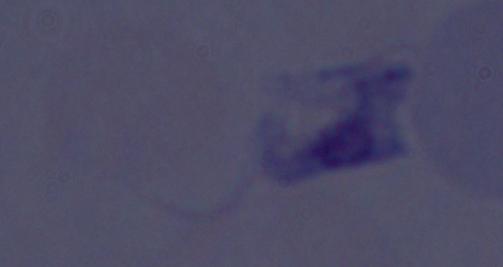

{
  "identification": "trypanosome",
  "modality": "photomicrograph",
  "magnification": "1000x"
}